Classify this cell by malaria status.
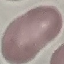
Uninfected.

stain = Giemsa
preparation = thin blood film
capture = smartphone through the microscope eyepiece
image type = cell patch, automatically extracted from a larger field of view and resized to 64 × 64 pixels